Classify this cell by malaria status.
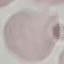

It is uninfected.

stain = Giemsa
capture = smartphone camera at the microscope eyepiece
image type = automatically extracted cell patch, resized to 64 × 64 pixels
preparation = thin blood film